Assess for malaria.
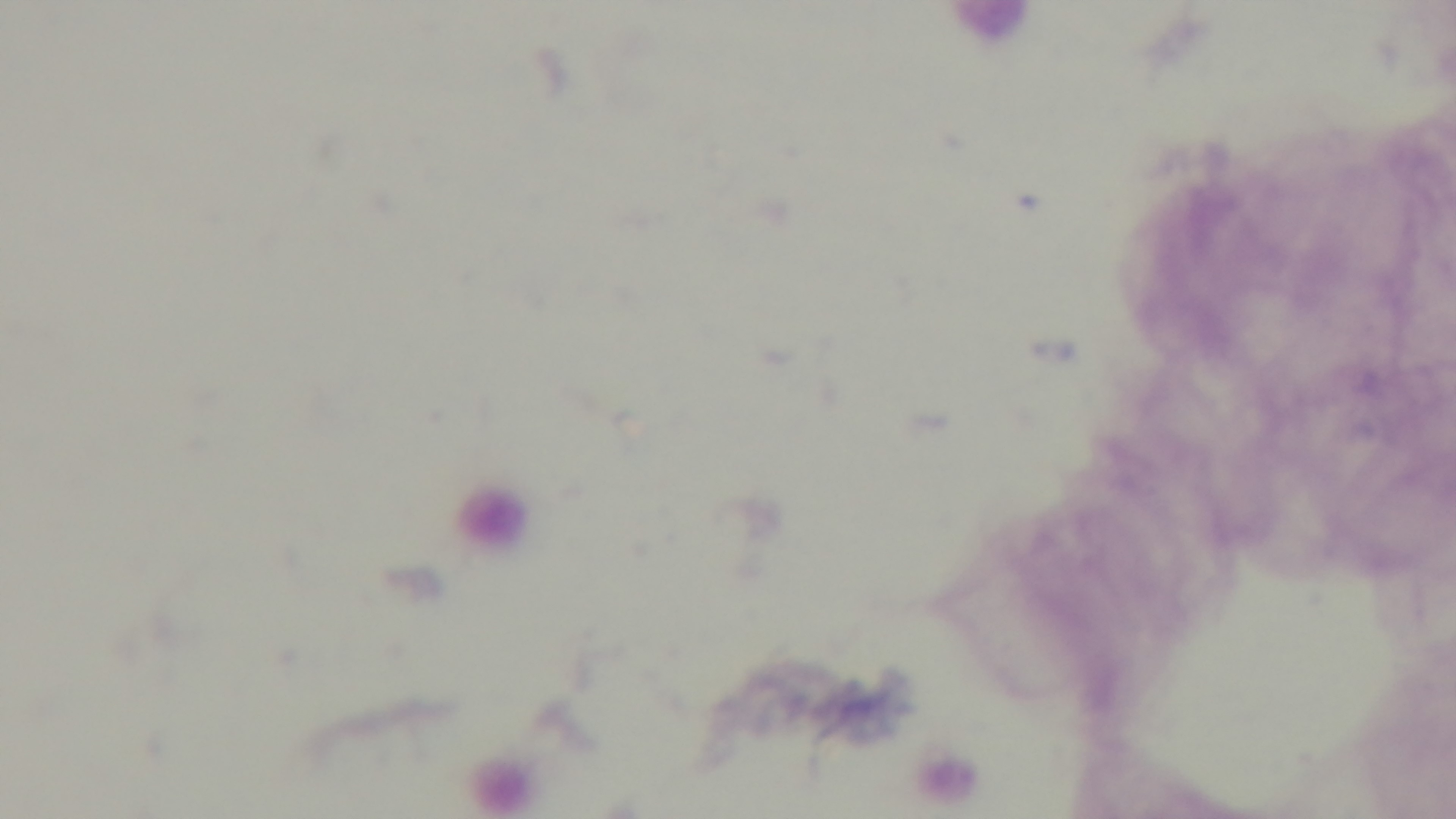
Uninfected.

Preparation: thick. Mounted 4K digital camera. Giemsa stain. 100x oil-immersion objective. Light microscopy. Single field of view.